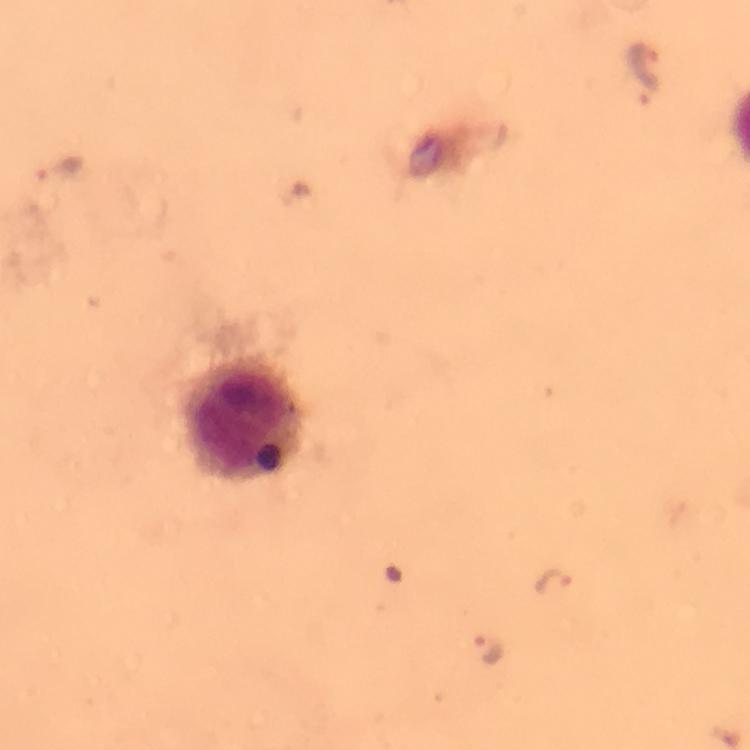 Approximate centers as {x, y} in pixels. Malaria parasite locations: {647, 71}, {551, 582}, {488, 646}. Leukocyte locations: {245, 420}. Giemsa-stained preparation. A crop from one field of view. 100x magnification. Photographed through the microscope with a smartphone camera. Image is 750×750 pixels. From a malaria diagnostic workup. Immersion oil was used. Thick blood film.